Classify this cell by malaria status.
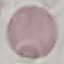
It is uninfected.

Cell patch, automatically extracted from a larger field of view and resized to 64 × 64 pixels. Photographed with a smartphone camera at the microscope eyepiece. Thin blood smear. Giemsa-stained preparation.